Classify this cell by malaria status.
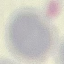
Uninfected.

Automatically extracted cell patch, resized to 64 × 64 pixels. Thin smear of blood. Giemsa stain. Acquired by smartphone through the microscope eyepiece.